State which cell type is depicted.
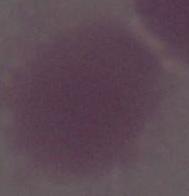

An erythrocyte.

Captured at 1000x magnification. Photomicrograph.